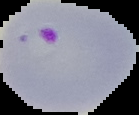

image type = segmented cell region with the area outside set to black
preparation = thin blood film
image size = 139×115 pixels
result = malaria parasites detected